Classify this cell by malaria status.
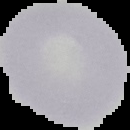
Uninfected.

image type = segmented cell region with the area outside set to black
preparation = thin blood smear
image size = 130×130 pixels